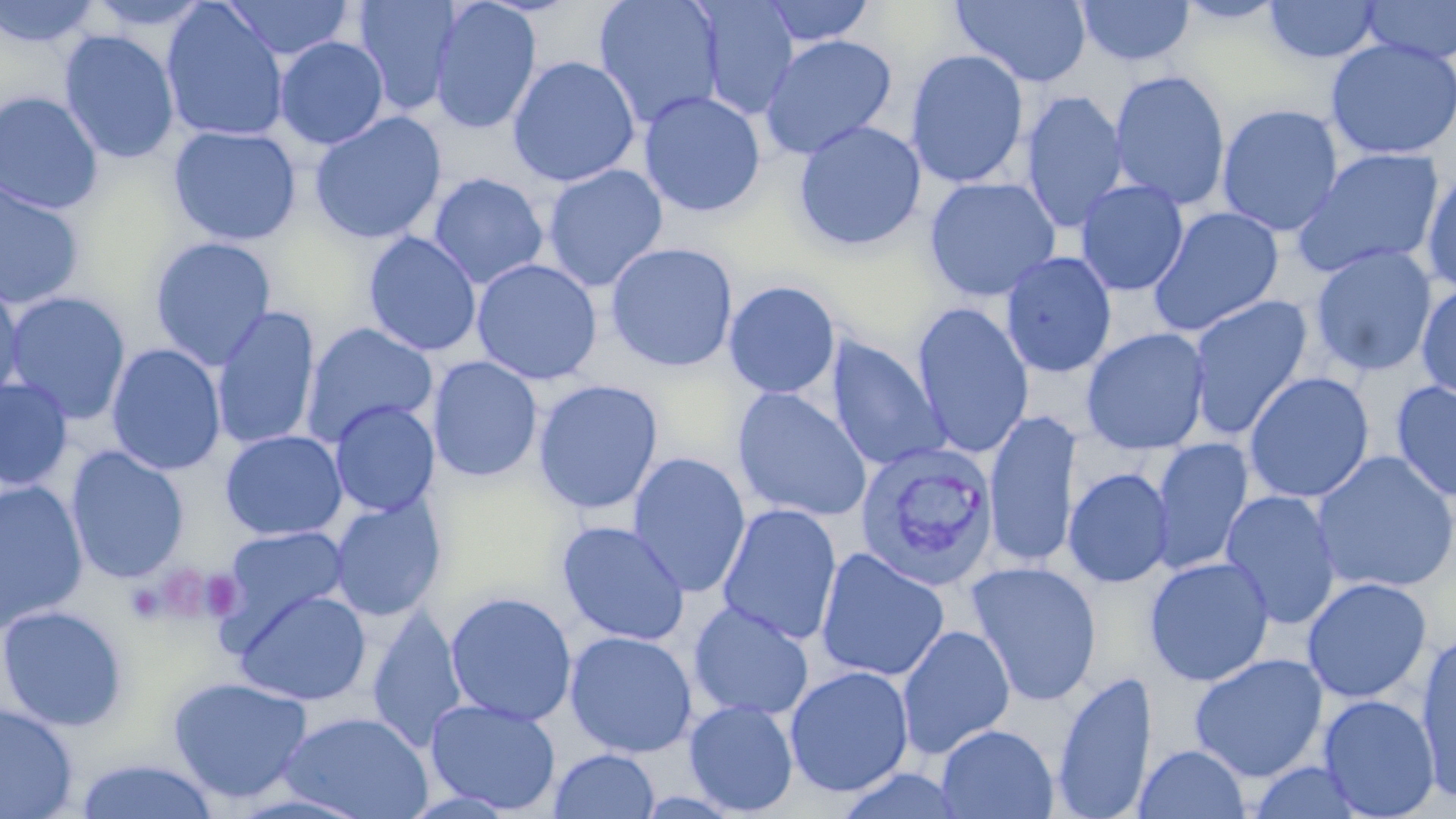

Approximate bounding boxes as named x1/y1/x2/y2 corners in pixels. Plasmodium vivax-infected red blood cell locations: (x1=854, y1=442, x2=1000, y2=591). Platelet locations: (x1=152, y1=563, x2=221, y2=623), (x1=125, y1=583, x2=167, y2=624). Uninfected red blood cell locations: (x1=0, y1=0, x2=99, y2=48), (x1=83, y1=0, x2=213, y2=31), (x1=221, y1=0, x2=353, y2=60), (x1=351, y1=0, x2=461, y2=116), (x1=428, y1=0, x2=542, y2=136), (x1=593, y1=0, x2=724, y2=129), (x1=759, y1=0, x2=876, y2=48), (x1=951, y1=0, x2=1092, y2=87), (x1=1077, y1=0, x2=1195, y2=67), (x1=1174, y1=0, x2=1288, y2=26), (x1=1359, y1=0, x2=1456, y2=64), (x1=695, y1=1, x2=800, y2=120), (x1=1264, y1=1, x2=1382, y2=63), (x1=161, y1=2, x2=289, y2=143), (x1=59, y1=30, x2=180, y2=164), (x1=760, y1=34, x2=898, y2=160), (x1=274, y1=36, x2=389, y2=150), (x1=1324, y1=38, x2=1456, y2=161), (x1=905, y1=49, x2=1029, y2=189), (x1=507, y1=55, x2=640, y2=187), (x1=1109, y1=69, x2=1231, y2=212), (x1=639, y1=90, x2=766, y2=217), (x1=1020, y1=90, x2=1128, y2=234), (x1=0, y1=91, x2=104, y2=215), (x1=1216, y1=104, x2=1344, y2=236), (x1=309, y1=111, x2=447, y2=244), (x1=792, y1=119, x2=927, y2=252), (x1=168, y1=125, x2=301, y2=246), (x1=1291, y1=147, x2=1447, y2=278), (x1=542, y1=164, x2=668, y2=293), (x1=1421, y1=167, x2=1456, y2=295), (x1=428, y1=172, x2=549, y2=289), (x1=924, y1=176, x2=1061, y2=302), (x1=1075, y1=179, x2=1189, y2=296), (x1=0, y1=182, x2=85, y2=311), (x1=1147, y1=205, x2=1285, y2=338), (x1=363, y1=231, x2=482, y2=357), (x1=148, y1=236, x2=277, y2=371), (x1=605, y1=242, x2=739, y2=373), (x1=1308, y1=244, x2=1438, y2=378), (x1=1000, y1=251, x2=1117, y2=378), (x1=471, y1=258, x2=602, y2=385), (x1=0, y1=278, x2=25, y2=406), (x1=723, y1=280, x2=841, y2=399), (x1=1415, y1=283, x2=1456, y2=402), (x1=3, y1=291, x2=132, y2=425), (x1=1186, y1=295, x2=1313, y2=441), (x1=911, y1=302, x2=1034, y2=458), (x1=212, y1=305, x2=320, y2=451), (x1=301, y1=323, x2=438, y2=447), (x1=1081, y1=327, x2=1211, y2=453), (x1=825, y1=338, x2=949, y2=471), (x1=106, y1=343, x2=226, y2=476), (x1=427, y1=356, x2=542, y2=483), (x1=1243, y1=371, x2=1375, y2=503), (x1=0, y1=378, x2=73, y2=491), (x1=533, y1=380, x2=664, y2=515), (x1=1390, y1=380, x2=1456, y2=504), (x1=731, y1=387, x2=873, y2=523), (x1=329, y1=400, x2=440, y2=517), (x1=984, y1=410, x2=1081, y2=570), (x1=220, y1=429, x2=348, y2=541), (x1=1149, y1=438, x2=1254, y2=576), (x1=65, y1=446, x2=190, y2=585), (x1=1311, y1=450, x2=1456, y2=593), (x1=628, y1=452, x2=751, y2=598), (x1=1063, y1=467, x2=1174, y2=589), (x1=0, y1=481, x2=89, y2=631), (x1=1220, y1=489, x2=1341, y2=630), (x1=329, y1=496, x2=446, y2=622), (x1=717, y1=503, x2=842, y2=647), (x1=556, y1=520, x2=691, y2=646), (x1=222, y1=525, x2=349, y2=633), (x1=815, y1=547, x2=950, y2=683), (x1=1144, y1=556, x2=1274, y2=687), (x1=965, y1=560, x2=1103, y2=707), (x1=1301, y1=577, x2=1433, y2=704), (x1=233, y1=589, x2=371, y2=705), (x1=445, y1=591, x2=577, y2=726), (x1=688, y1=601, x2=814, y2=721), (x1=0, y1=605, x2=128, y2=731), (x1=367, y1=607, x2=468, y2=752), (x1=896, y1=625, x2=1015, y2=759), (x1=1415, y1=627, x2=1456, y2=802), (x1=565, y1=630, x2=697, y2=758), (x1=1189, y1=653, x2=1328, y2=782), (x1=784, y1=665, x2=914, y2=798), (x1=1052, y1=669, x2=1157, y2=819), (x1=167, y1=675, x2=314, y2=805), (x1=1318, y1=694, x2=1440, y2=818), (x1=425, y1=698, x2=561, y2=815), (x1=685, y1=699, x2=798, y2=816), (x1=0, y1=702, x2=79, y2=819), (x1=277, y1=711, x2=434, y2=819), (x1=936, y1=724, x2=1058, y2=819), (x1=1135, y1=744, x2=1250, y2=818), (x1=549, y1=749, x2=659, y2=819), (x1=73, y1=757, x2=220, y2=818), (x1=1246, y1=761, x2=1369, y2=819). Slide-level diagnosis: Plasmodium vivax. Thin blood film. Image is 1456×819 pixels. Light microscopy. Captured at 1000x magnification. May-Grünwald-Giemsa stain. Single field of view.